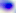
Summary:
  - Magnification: 400x
  - Modality: photomicrograph
  - Identification: Toxoplasma gondii